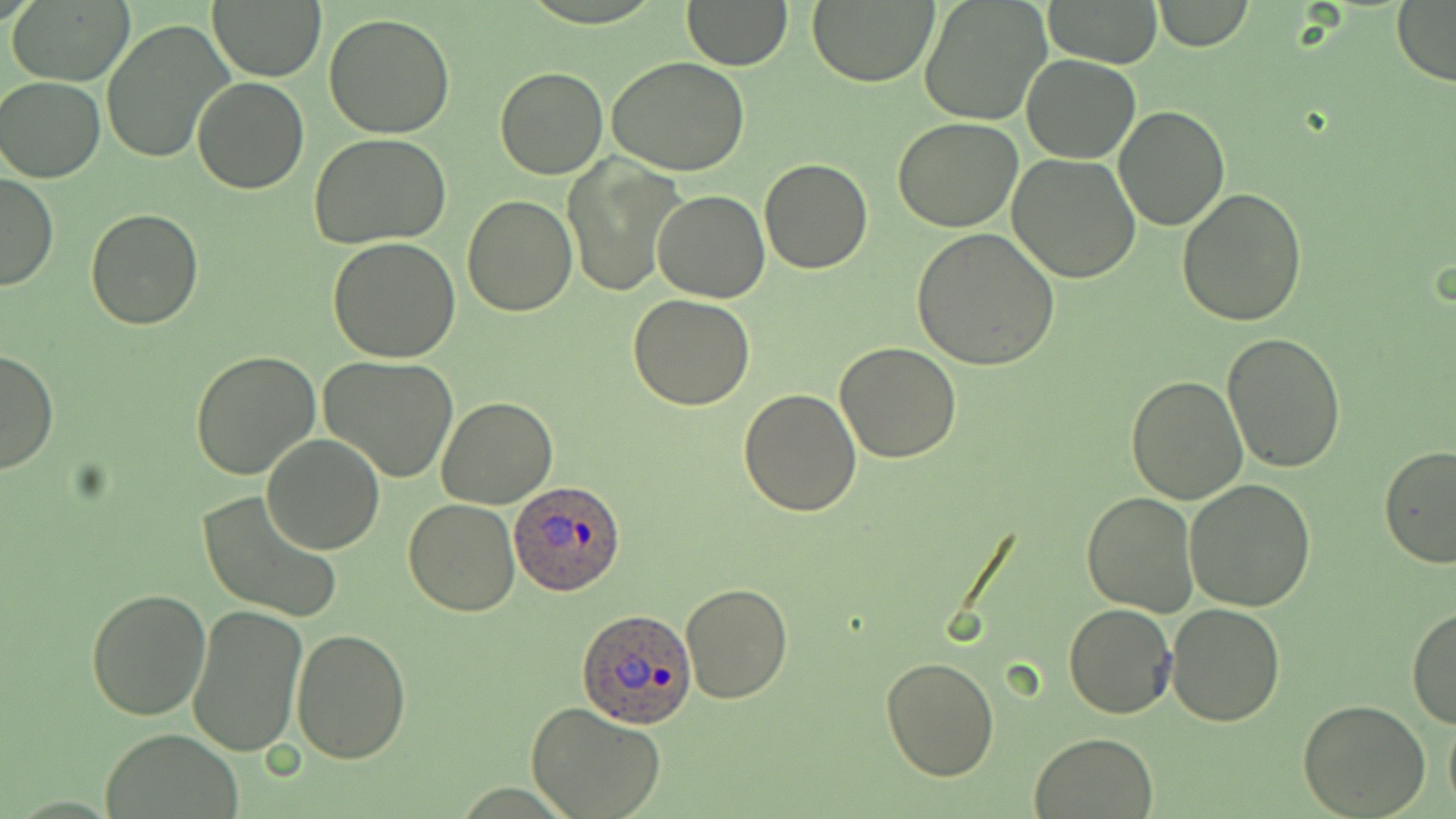

Approximate bounding boxes as (x1, y1, x2, y2) in pixels. Plasmodium ovale-infected red blood cell locations: (508, 479, 628, 595), (577, 608, 699, 731). Uninfected red blood cell locations: (805, 0, 939, 87), (919, 0, 1052, 125), (1045, 0, 1163, 68), (10, 1, 134, 86), (208, 1, 326, 81), (684, 1, 792, 70), (1150, 1, 1253, 51), (1391, 3, 1456, 83), (324, 13, 457, 137), (101, 19, 236, 165), (1022, 54, 1141, 163), (607, 56, 751, 175), (495, 68, 608, 179), (192, 74, 309, 194), (1, 76, 105, 182), (1114, 105, 1229, 230), (894, 118, 1024, 232), (309, 134, 452, 249), (1009, 153, 1142, 283), (760, 158, 872, 274), (563, 159, 685, 298), (0, 175, 58, 290), (1176, 187, 1308, 326), (652, 189, 769, 304), (463, 195, 576, 316), (84, 208, 202, 329), (911, 228, 1060, 371), (327, 237, 460, 361), (627, 293, 757, 410), (1223, 331, 1346, 472), (834, 341, 963, 462), (0, 349, 58, 475), (189, 350, 321, 482), (320, 355, 458, 483), (1126, 374, 1250, 505), (737, 387, 863, 516), (436, 396, 559, 510), (262, 433, 383, 554), (1375, 445, 1456, 568), (1185, 478, 1316, 612), (1081, 490, 1199, 617), (197, 491, 342, 621), (404, 499, 521, 617), (680, 581, 792, 703), (85, 587, 212, 720), (1063, 600, 1177, 720), (187, 603, 309, 758), (1167, 603, 1285, 726), (1406, 606, 1455, 730), (292, 628, 412, 766), (880, 656, 999, 780), (1299, 699, 1429, 818), (526, 701, 665, 819), (1443, 710, 1456, 814), (98, 729, 246, 819), (1030, 730, 1159, 818). Slide-level diagnosis: Plasmodium ovale. Single field of view. Light microscopy. Image is 1456×819 pixels. Thin blood smear. May-Grünwald-Giemsa stain. 1000x magnification.